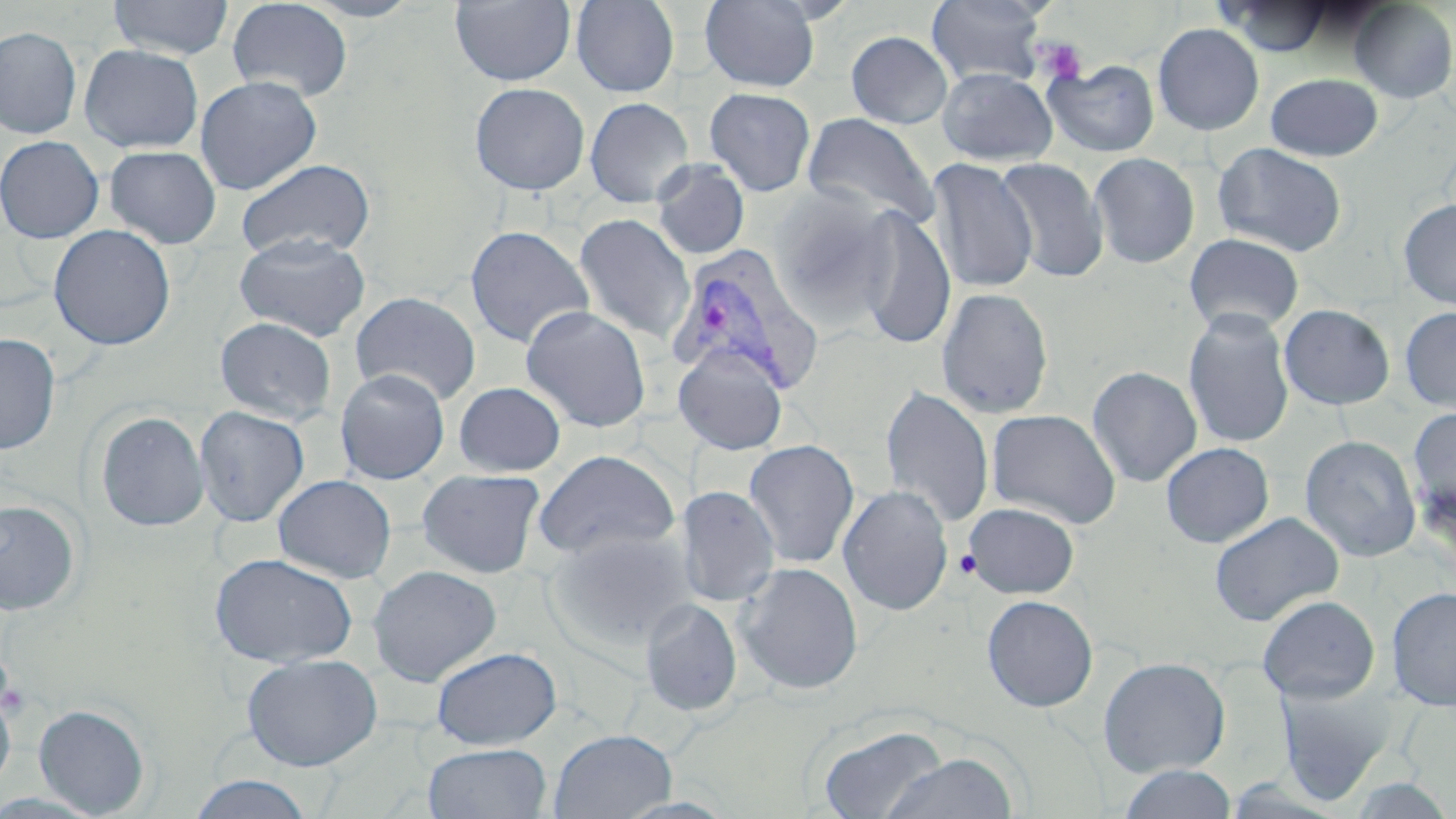
Summary:
  - Coordinate format: approximate bounding boxes as [x1, y1, x2, y2] in pixels
  - Platelet locations: [1033, 37, 1088, 85], [954, 549, 980, 579], [1, 660, 25, 721]
  - Plasmodium vivax-infected red blood cell locations: [668, 246, 824, 395]
  - Uninfected red blood cell locations: [107, 0, 235, 60], [226, 0, 353, 101], [297, 0, 425, 22], [570, 0, 680, 98], [926, 0, 1049, 88], [450, 1, 576, 86], [699, 1, 821, 92], [1219, 1, 1333, 56], [1349, 1, 1456, 103], [1152, 23, 1265, 136], [0, 26, 82, 139], [845, 30, 954, 129], [79, 44, 204, 153], [1043, 59, 1161, 158], [936, 68, 1057, 166], [1265, 73, 1383, 161], [194, 75, 322, 195], [469, 82, 590, 195], [704, 87, 816, 196], [584, 96, 694, 208], [801, 112, 940, 231], [0, 135, 105, 243], [1212, 142, 1348, 257], [104, 145, 222, 249], [1088, 151, 1201, 269], [994, 157, 1109, 283], [235, 158, 376, 260], [927, 158, 1039, 292], [650, 159, 750, 260], [765, 188, 901, 331], [1397, 199, 1456, 310], [853, 206, 957, 350], [574, 213, 694, 344], [48, 224, 176, 350], [464, 224, 594, 349], [233, 233, 371, 342], [1183, 233, 1305, 336], [935, 287, 1055, 419], [350, 291, 482, 406], [1279, 304, 1395, 410], [520, 305, 652, 433], [1399, 306, 1456, 413], [1182, 308, 1295, 450], [214, 316, 337, 424], [0, 333, 61, 454], [672, 343, 789, 455], [1087, 365, 1202, 487], [335, 368, 450, 484], [453, 381, 566, 477], [879, 385, 995, 528], [193, 406, 310, 527], [1406, 406, 1456, 530], [985, 407, 1122, 529], [94, 410, 210, 532], [1299, 435, 1422, 562], [743, 439, 860, 568], [1160, 442, 1274, 548], [532, 449, 681, 563], [416, 468, 546, 579], [272, 474, 397, 583], [838, 484, 954, 616], [675, 485, 780, 607], [0, 499, 82, 615], [963, 502, 1080, 598], [1209, 511, 1344, 626], [546, 528, 694, 652], [208, 552, 359, 668], [734, 561, 864, 695], [367, 564, 502, 686], [1386, 586, 1456, 710], [981, 594, 1099, 713], [1257, 595, 1381, 703], [639, 598, 743, 718], [431, 646, 562, 750], [241, 653, 383, 771], [1097, 656, 1231, 777], [1274, 679, 1395, 803], [0, 685, 16, 796], [33, 703, 151, 818], [818, 723, 948, 819], [548, 729, 676, 819], [423, 742, 552, 819], [882, 752, 1018, 818], [1118, 764, 1238, 819], [186, 774, 315, 818]
  - Slide-level diagnosis: Plasmodium vivax
  - Magnification: 1000x
  - Preparation: thin blood smear
  - Image size: 1456×819 pixels
  - Field of view: single
  - Modality: optical microscopy
  - Stain: May-Grünwald-Giemsa